Assess this cell for malaria.
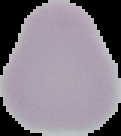

It is uninfected.

From a thin blood film. Cell region segmented out of the field of view; the surrounding area is masked to black. Image is 121×136 pixels.